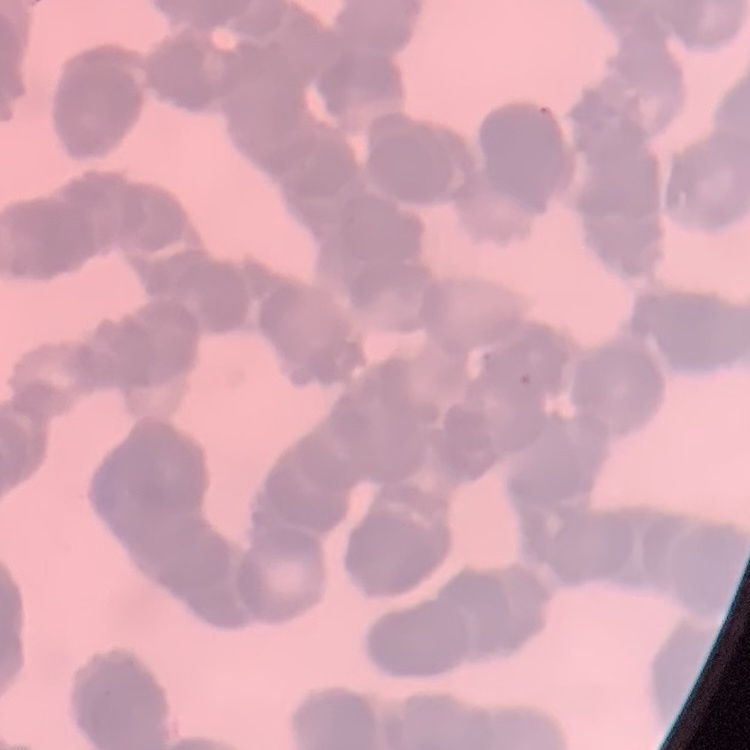

red blood cell morphology = rouleaux formation
stain = Field's or Giemsa
preparation = thin blood smear
image type = one tile cut from a larger photomicrograph